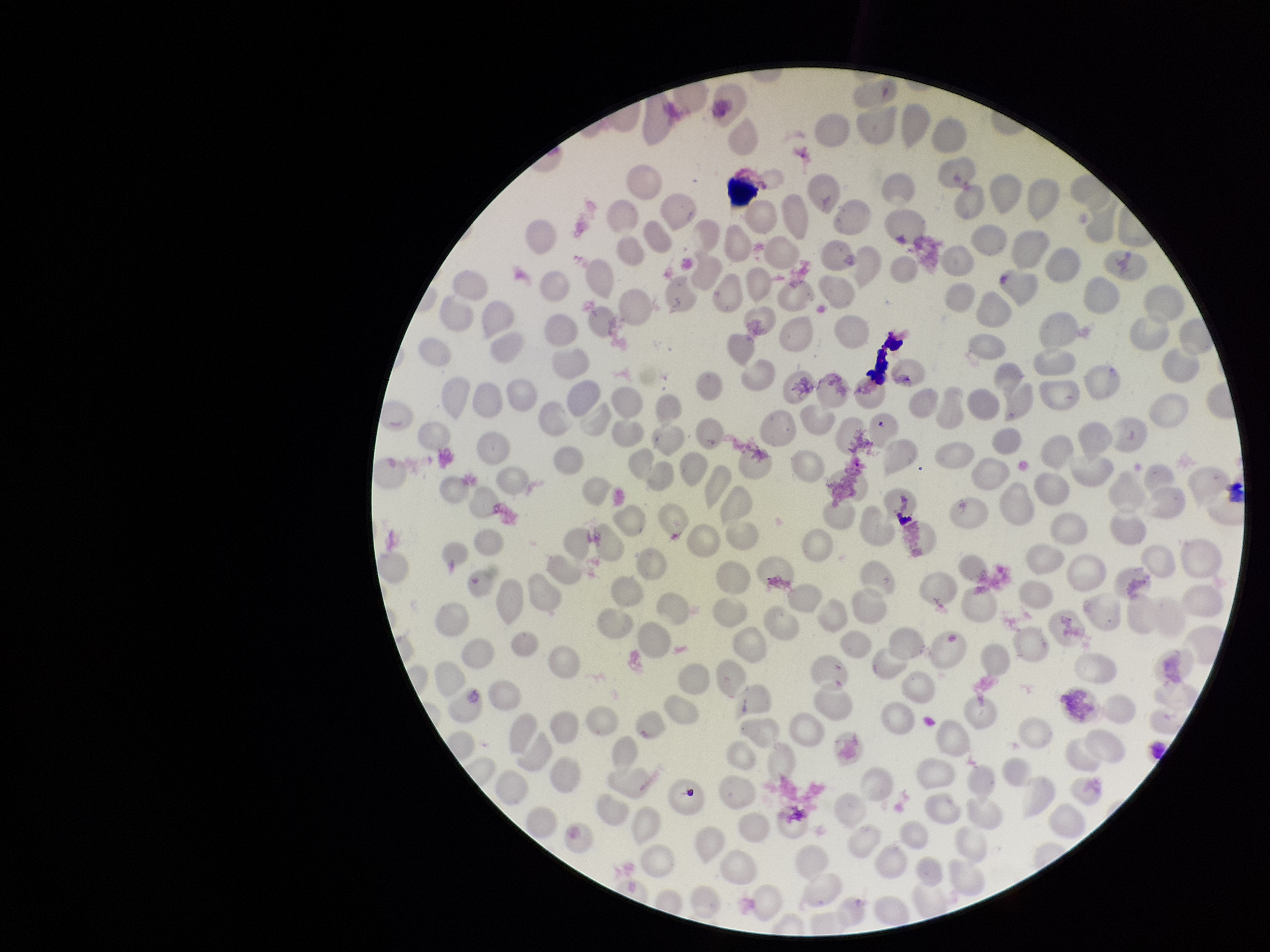

Summary:
  - Patient malaria status: infected
  - Capture: smartphone photograph through the microscope eyepiece
  - Red blood cell count: 271
  - Image size: 1270×952 pixels
  - Parasitized red blood cell count: 0
  - Parasitized red blood cells: none seen
  - Species reported for this patient: Plasmodium vivax
  - Stain: Giemsa
  - Field of view: one from this slide
  - Preparation: thin blood smear